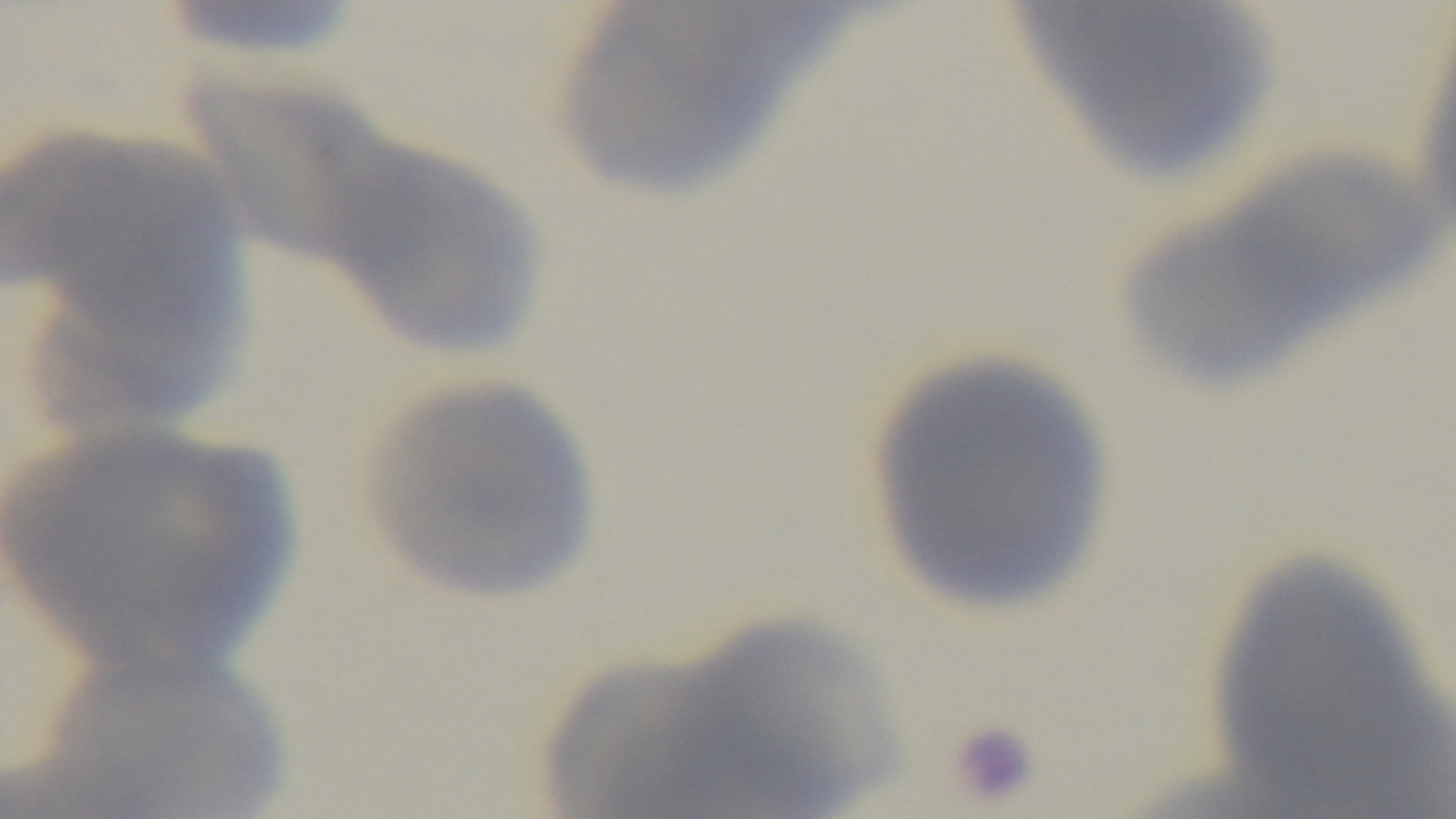 Mounted 4K digital camera. Giemsa-stained. Photomicrograph. Malaria status: negative. 100x oil-immersion objective. Single field of view. Preparation: thin smear.